Comment on the morphology of the erythrocytes.
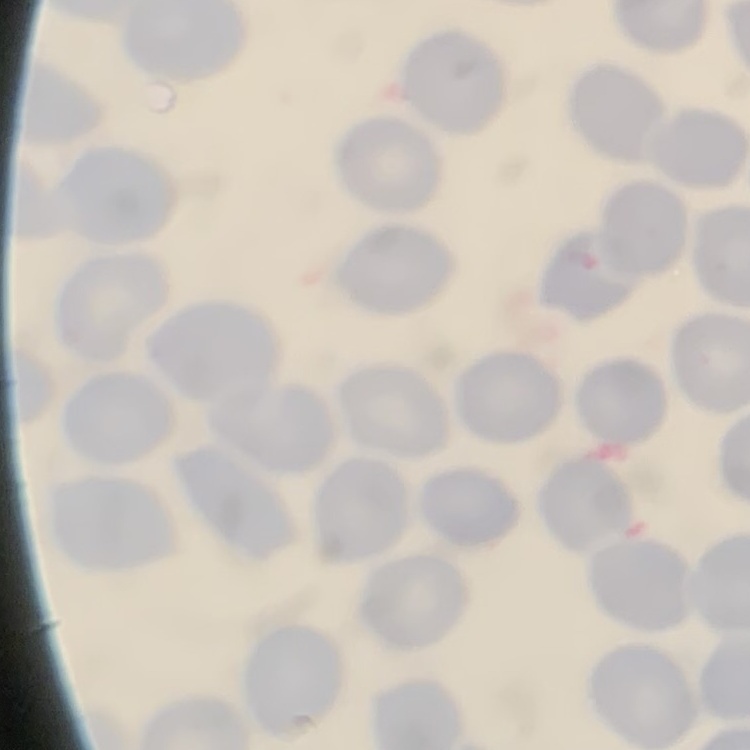
No rouleaux formation.

Summary:
  - Stain: Field's or Giemsa
  - Image type: one tile cut from a larger photomicrograph
  - Preparation: thin peripheral smear